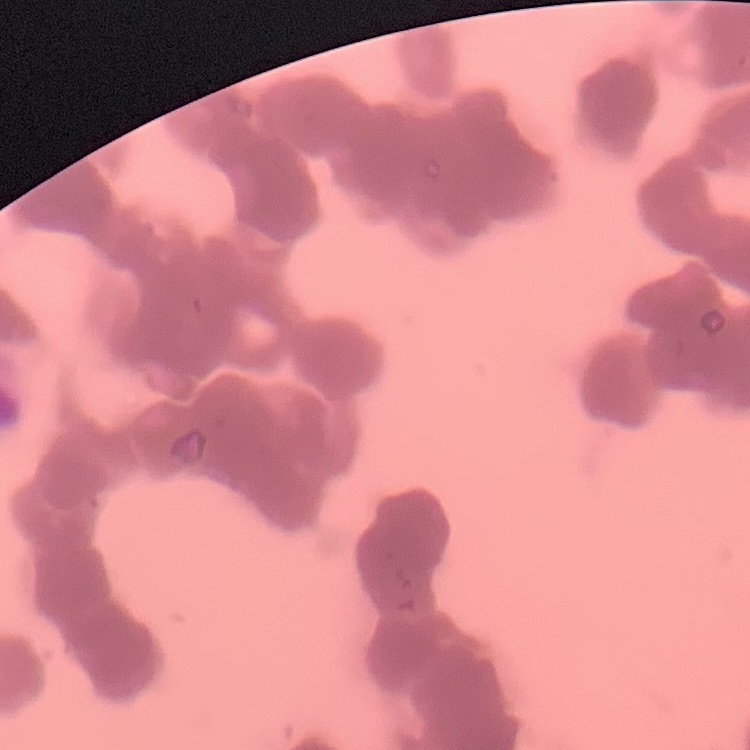

erythrocyte morphology = rouleaux formation
preparation = thin blood smear
stain = Field's or Giemsa
image type = square crop of a larger photomicrograph